Give the extent of all uninfected red blood cells.
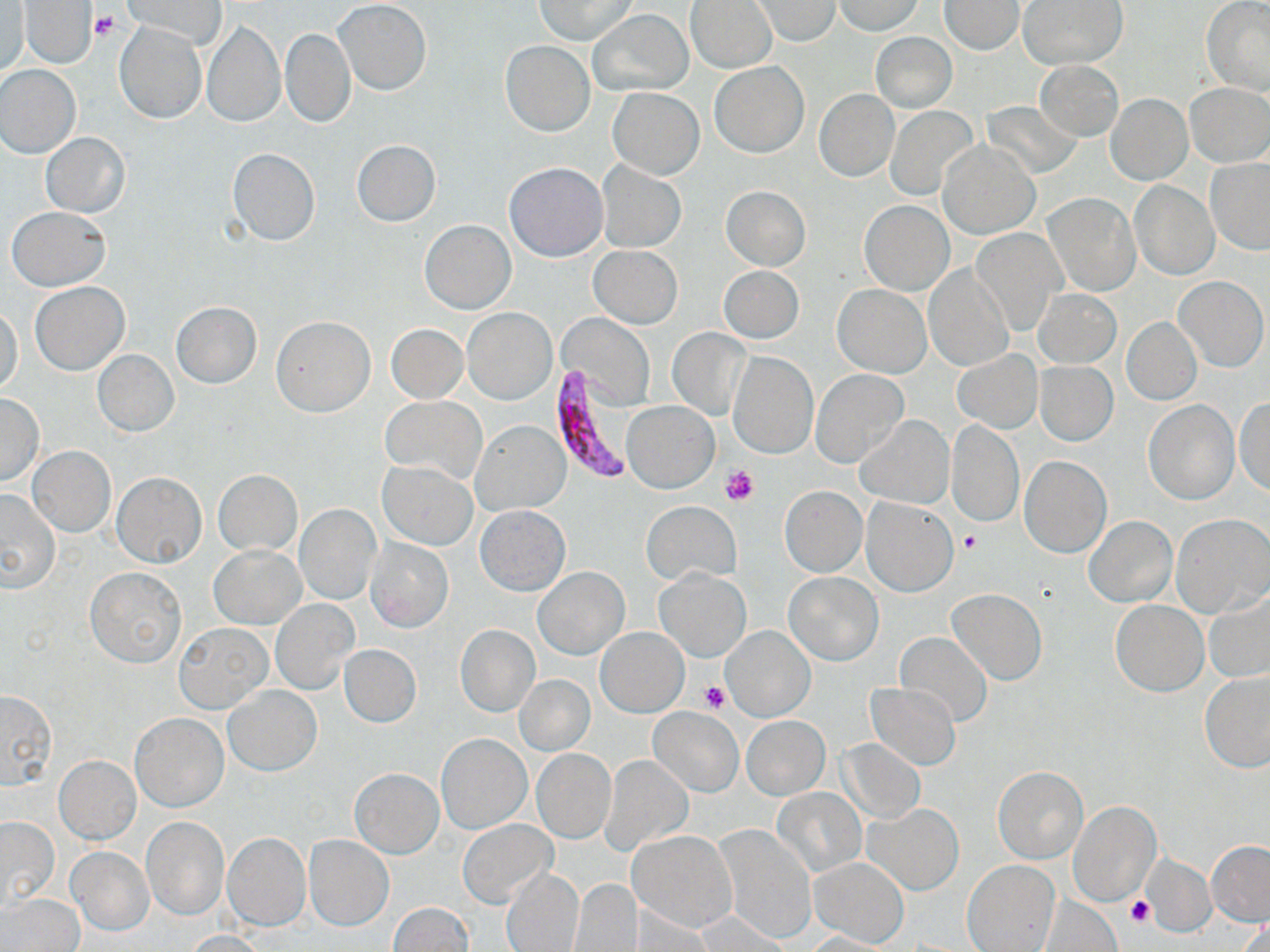
Approximate bounding boxes as (x1, y1, x2, y2) in pixels.
Uninfected red blood cells: (124, 0, 227, 49), (534, 0, 638, 44), (750, 0, 841, 45), (21, 1, 97, 67), (334, 1, 431, 95), (686, 1, 778, 74), (832, 1, 923, 35), (939, 1, 1023, 55), (1018, 1, 1127, 70), (1203, 1, 1270, 97), (2, 6, 29, 75), (589, 11, 692, 95), (202, 20, 284, 127), (115, 22, 207, 123), (281, 27, 354, 127), (871, 32, 957, 112), (501, 40, 594, 136), (1034, 60, 1124, 141), (710, 62, 809, 158), (0, 65, 81, 158), (1186, 84, 1270, 166), (609, 87, 703, 179), (814, 89, 898, 182), (1105, 93, 1192, 185), (983, 100, 1082, 179), (885, 106, 978, 198), (41, 132, 129, 218), (352, 140, 442, 226), (938, 140, 1040, 237), (228, 148, 319, 245), (1205, 158, 1270, 255), (596, 161, 685, 253), (504, 162, 608, 261), (1129, 180, 1219, 280), (721, 186, 810, 271), (1045, 193, 1139, 295), (860, 200, 954, 296), (6, 207, 111, 291), (420, 220, 515, 314), (971, 228, 1067, 333), (590, 245, 682, 327), (924, 264, 1014, 371), (719, 265, 803, 343), (1173, 275, 1268, 372), (29, 281, 130, 376), (833, 284, 932, 377), (1034, 290, 1121, 368), (170, 302, 262, 388), (1, 306, 24, 396), (462, 306, 556, 405), (558, 314, 655, 404), (271, 317, 375, 416), (1122, 318, 1201, 405), (387, 324, 467, 403), (667, 328, 749, 419), (93, 350, 178, 437), (950, 350, 1042, 434), (728, 351, 816, 458), (1035, 361, 1118, 445), (812, 369, 909, 468), (0, 392, 44, 486), (381, 397, 486, 484), (1234, 399, 1270, 496), (623, 400, 718, 493), (1144, 400, 1239, 504), (857, 416, 953, 509), (946, 419, 1024, 527), (473, 420, 570, 514), (26, 446, 115, 537), (1020, 456, 1111, 557), (378, 462, 477, 549), (213, 468, 302, 556), (112, 471, 206, 567), (779, 486, 866, 577), (0, 487, 60, 594), (863, 498, 958, 596), (642, 500, 741, 586), (294, 505, 380, 605), (475, 505, 571, 596), (1085, 515, 1177, 606), (1170, 515, 1269, 618), (365, 538, 454, 633), (209, 545, 305, 629), (85, 567, 186, 667), (534, 567, 628, 660), (655, 568, 750, 661), (783, 572, 883, 664), (948, 588, 1047, 684), (1205, 590, 1270, 684), (271, 599, 358, 694), (1111, 600, 1208, 697), (175, 623, 272, 713), (455, 624, 540, 717), (721, 625, 814, 721), (597, 627, 688, 717), (894, 630, 992, 727), (338, 644, 421, 727), (1198, 670, 1270, 773), (515, 675, 594, 755), (865, 682, 961, 771), (224, 685, 321, 776), (0, 690, 57, 789), (648, 706, 743, 797), (130, 713, 228, 811), (741, 716, 829, 799), (437, 733, 531, 833), (839, 739, 926, 824), (531, 747, 616, 844), (603, 755, 693, 854), (54, 756, 141, 843), (993, 767, 1087, 863), (350, 768, 443, 857), (774, 788, 866, 877), (1069, 802, 1160, 905), (865, 803, 964, 895), (0, 817, 60, 910), (141, 817, 228, 920), (458, 819, 556, 910), (716, 824, 817, 944), (629, 829, 736, 932), (222, 833, 310, 930), (303, 835, 395, 931), (1205, 841, 1270, 926), (67, 847, 153, 934), (1142, 855, 1216, 936), (809, 858, 909, 947), (963, 860, 1059, 951), (500, 867, 584, 952), (570, 880, 642, 952), (2, 894, 84, 952), (1036, 896, 1122, 951), (387, 902, 475, 952), (626, 908, 715, 948), (696, 911, 792, 949), (1235, 919, 1270, 952), (186, 930, 269, 951), (804, 931, 896, 951).

{
  "slide_level_diagnosis": "Plasmodium falciparum",
  "stain": "May-Grünwald-Giemsa",
  "plasmodium_falciparum_infected_red_blood_cell_locations": "approximate bounding boxes as (x1, y1, x2, y2) in pixels: (551, 365, 636, 485)",
  "platelet_locations": "approximate bounding boxes as (x1, y1, x2, y2) in pixels: (91, 11, 119, 40), (720, 464, 761, 507), (958, 530, 983, 554), (700, 679, 730, 713), (1125, 894, 1154, 927)",
  "preparation": "thin blood smear",
  "magnification": "1000x",
  "field_of_view": "single",
  "image_size": "1270×952 pixels",
  "modality": "light microscopy"
}